Report the malaria status of this cell.
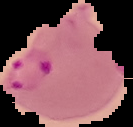
It is parasitized.

From a thin blood smear. Image is 133×127 pixels. Cell region segmented out of the field of view; the surrounding area is masked to black.